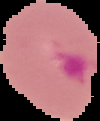
The area outside the segmented cell region is set to black. Image is 100×121 pixels. Malaria status: parasitized. From a thin blood smear.